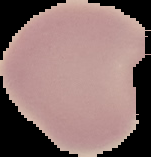 The area outside the segmented cell region is set to black. Image is 151×157 pixels. Malaria status: uninfected. From a thin blood film.